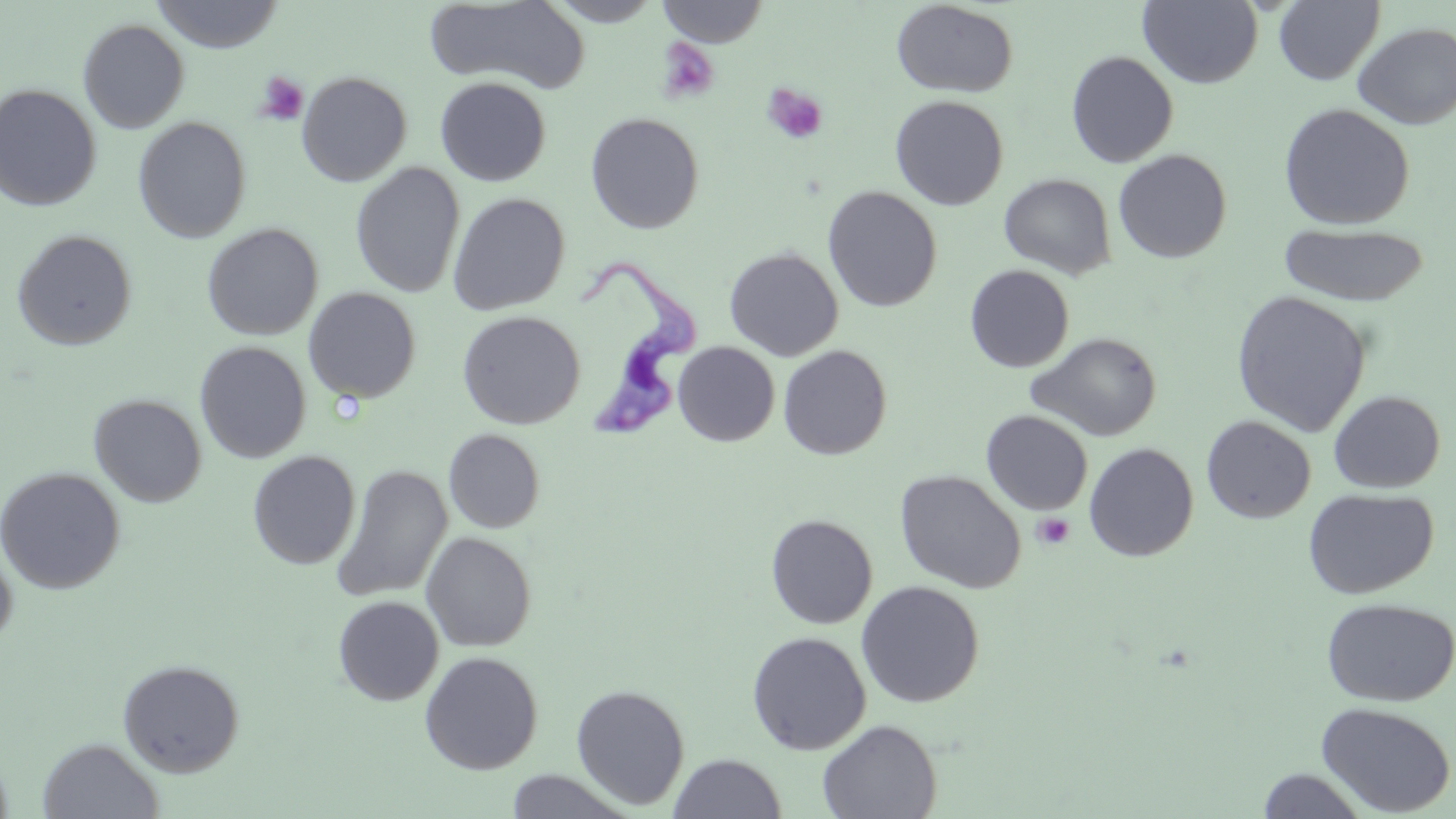
Summary:
  - Coordinate format: approximate bounding boxes as (x1,y1)-(x2,y2) corner pairs in pixels
  - Trypanosoma brucei locations: (579,260)-(701,440)
  - Platelet locations: (656,37)-(720,104), (255,71)-(309,126), (762,83)-(828,145), (1032,513)-(1075,549)
  - Uninfected red blood cell locations: (151,0)-(284,53), (543,0)-(666,26), (657,0)-(769,47), (890,1)-(1019,98), (1138,1)-(1263,88), (1274,1)-(1385,86), (426,2)-(588,93), (78,19)-(190,134), (1353,22)-(1456,130), (1065,51)-(1179,168), (296,71)-(412,187), (435,77)-(552,187), (0,83)-(102,212), (890,95)-(1009,210), (1277,103)-(1415,230), (585,112)-(704,234), (133,117)-(251,243), (1113,149)-(1232,264), (350,162)-(465,298), (999,173)-(1116,280), (822,186)-(942,312), (448,192)-(570,315), (202,223)-(323,341), (1278,223)-(1431,306), (12,229)-(137,351), (724,246)-(844,361), (964,264)-(1075,373), (303,287)-(421,403), (1230,290)-(1372,437), (457,310)-(585,429), (1027,332)-(1162,441), (194,341)-(311,463), (673,342)-(780,446), (777,345)-(892,460), (1328,389)-(1446,493), (88,393)-(207,507), (981,410)-(1093,515), (1201,415)-(1317,524), (444,429)-(545,533), (1083,442)-(1199,561), (247,451)-(360,570), (331,464)-(453,603), (0,467)-(126,595), (894,470)-(1027,594), (1303,488)-(1439,599), (765,514)-(878,629), (421,531)-(537,651), (0,542)-(17,651), (856,580)-(985,708), (332,596)-(444,706), (1321,597)-(1456,707), (746,631)-(871,755), (419,651)-(543,775), (118,658)-(245,777), (571,683)-(690,810), (1315,701)-(1456,816), (817,718)-(942,818), (37,738)-(164,818), (669,753)-(786,818), (1256,768)-(1370,818), (505,770)-(635,818)
  - Slide-level diagnosis: Trypanosoma brucei
  - Image size: 1456×819 pixels
  - Field of view: single
  - Modality: light microscopy
  - Preparation: thin blood film
  - Magnification: 1000x
  - Stain: May-Grünwald-Giemsa